Assess this cell for malaria.
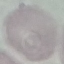

It is uninfected.

Acquired by smartphone through the microscope eyepiece. Automatically extracted cell patch, resized to 64 × 64 pixels. Thin smear of blood. Giemsa stain.